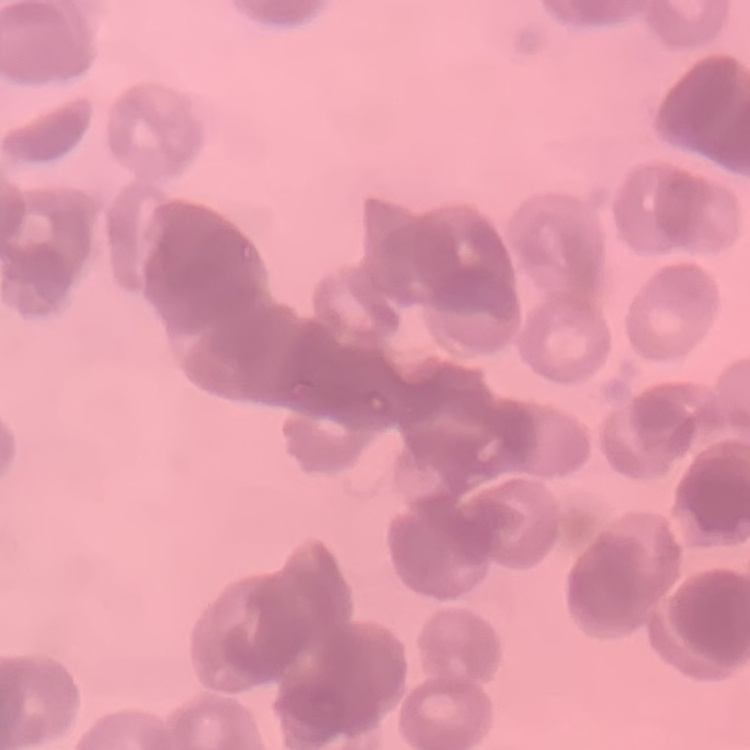

erythrocyte_morphology: rouleaux formation
preparation: thin blood film
stain: Field's or Giemsa
image_type: square crop of a larger photomicrograph